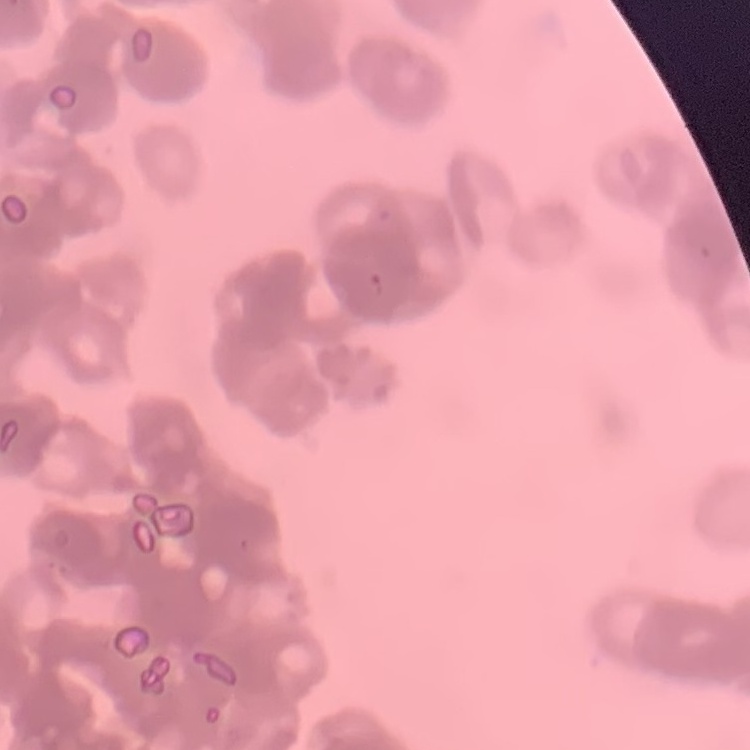
red_blood_cell_morphology: rouleaux formation
preparation: thin blood film
stain: Field's or Giemsa
image_type: square crop of a larger photomicrograph